Identify the cell.
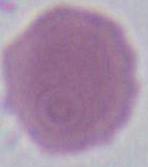
This is an erythrocyte.

modality = micrograph
magnification = 1000x